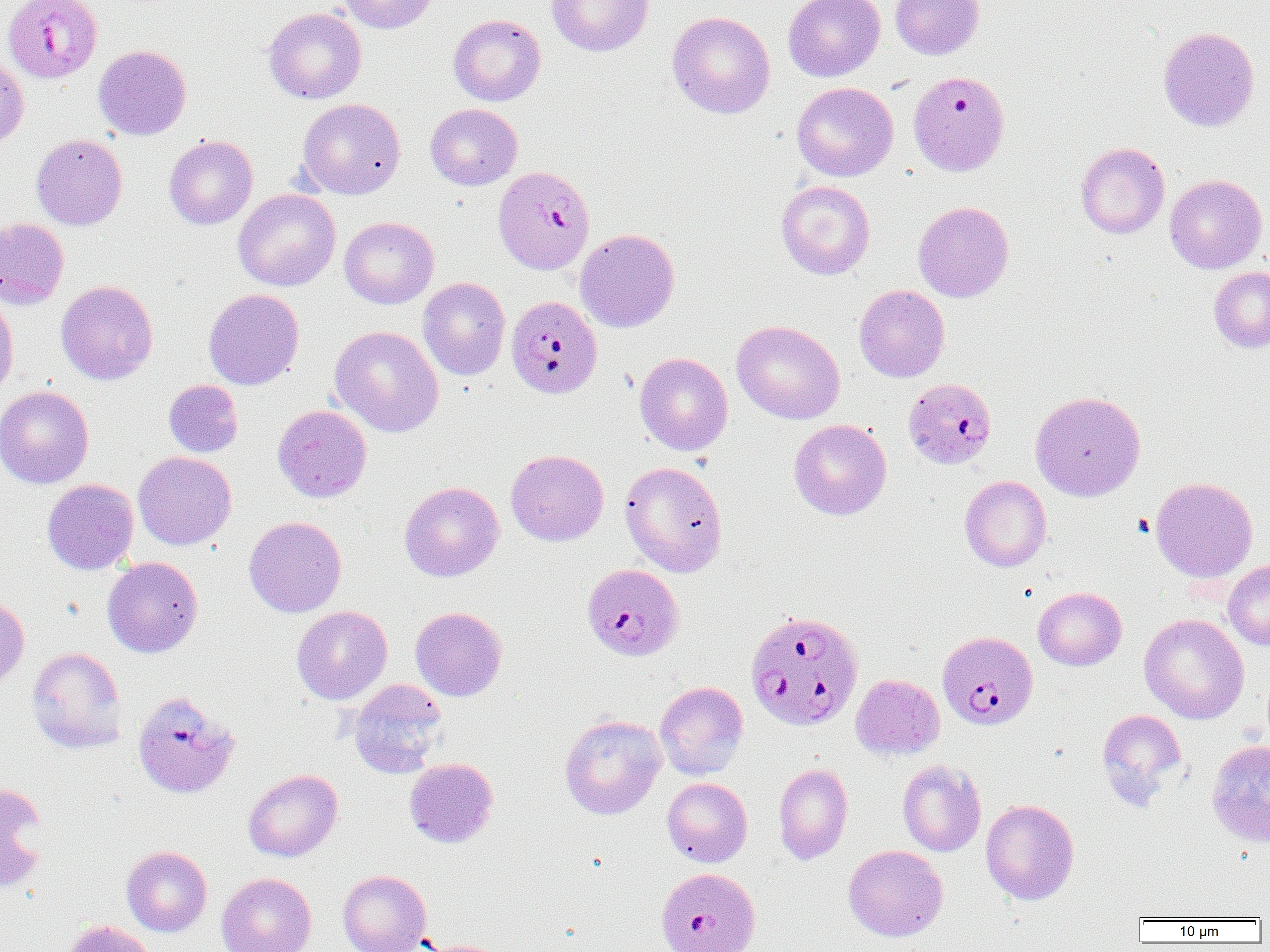 Approximate bounding boxes as (x1,y1)-(x2,y2) corner pairs in pixels. Uninfected red blood cell locations: (337,0)-(439,33), (547,0)-(654,56), (783,0)-(885,82), (890,0)-(985,60), (263,7)-(367,104), (667,11)-(775,118), (448,14)-(546,106), (1158,27)-(1260,132), (93,45)-(191,140), (0,53)-(29,149), (792,81)-(898,181), (297,98)-(406,199), (425,103)-(522,190), (31,134)-(127,231), (164,135)-(258,229), (1075,142)-(1170,239), (1165,174)-(1267,274), (776,180)-(875,280), (233,189)-(341,291), (913,201)-(1014,302), (339,216)-(438,309), (1,217)-(69,309), (575,228)-(680,332), (1209,266)-(1270,353), (418,277)-(511,380), (56,280)-(158,384), (854,285)-(950,382), (203,288)-(304,390), (0,290)-(19,401), (732,320)-(845,424), (330,325)-(444,437), (634,352)-(733,455), (163,379)-(243,457), (0,385)-(94,489), (1030,390)-(1146,501), (272,405)-(372,502), (790,419)-(892,525), (505,449)-(609,546), (134,451)-(236,550), (620,461)-(727,577), (960,476)-(1051,572), (1150,476)-(1258,583), (42,479)-(138,575), (399,481)-(504,582), (244,516)-(347,617), (102,556)-(203,657), (1223,561)-(1270,650), (1033,587)-(1126,671), (0,596)-(29,691), (291,606)-(392,705), (410,606)-(507,701), (1139,613)-(1249,724), (26,647)-(127,753), (851,674)-(945,760), (348,679)-(448,778), (654,681)-(749,780), (1096,708)-(1188,810), (559,714)-(666,819), (1206,739)-(1270,847), (404,758)-(499,848), (897,759)-(986,857), (773,763)-(853,865), (243,769)-(343,861), (662,777)-(753,867), (0,781)-(48,894), (980,798)-(1079,905), (843,845)-(948,941), (121,846)-(212,936), (337,869)-(431,952), (216,873)-(316,952), (60,919)-(159,952), (417,939)-(510,952). Plasmodium falciparum-infected red blood cell locations: (3,0)-(102,83), (907,70)-(1010,177), (493,165)-(595,275), (506,295)-(603,399), (903,378)-(997,470), (582,563)-(684,661), (746,613)-(865,734), (937,630)-(1039,730), (133,690)-(240,799), (654,869)-(759,952). Slide-level diagnosis: Plasmodium falciparum. One field of a larger specimen. Captured at 1000x magnification. Thin blood film. Image is 1270×952 pixels. Light microscopy.